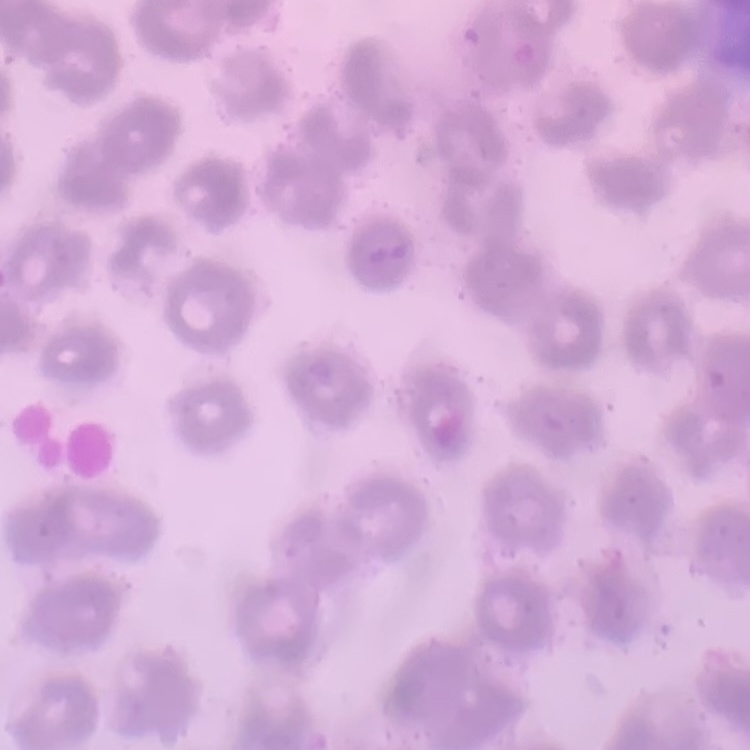
Summary:
  - Erythrocyte morphology: no rouleaux formation
  - Image type: square crop of a larger photomicrograph
  - Preparation: thin blood film
  - Stain: Field's or Giemsa